Report the malaria status of this cell.
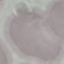

Uninfected.

Summary:
  - Stain: Giemsa
  - Preparation: thin smear
  - Capture: smartphone camera at the microscope eyepiece
  - Image type: automatically extracted cell patch, resized to 64 × 64 pixels